Give the extent of all uninfected red blood cells.
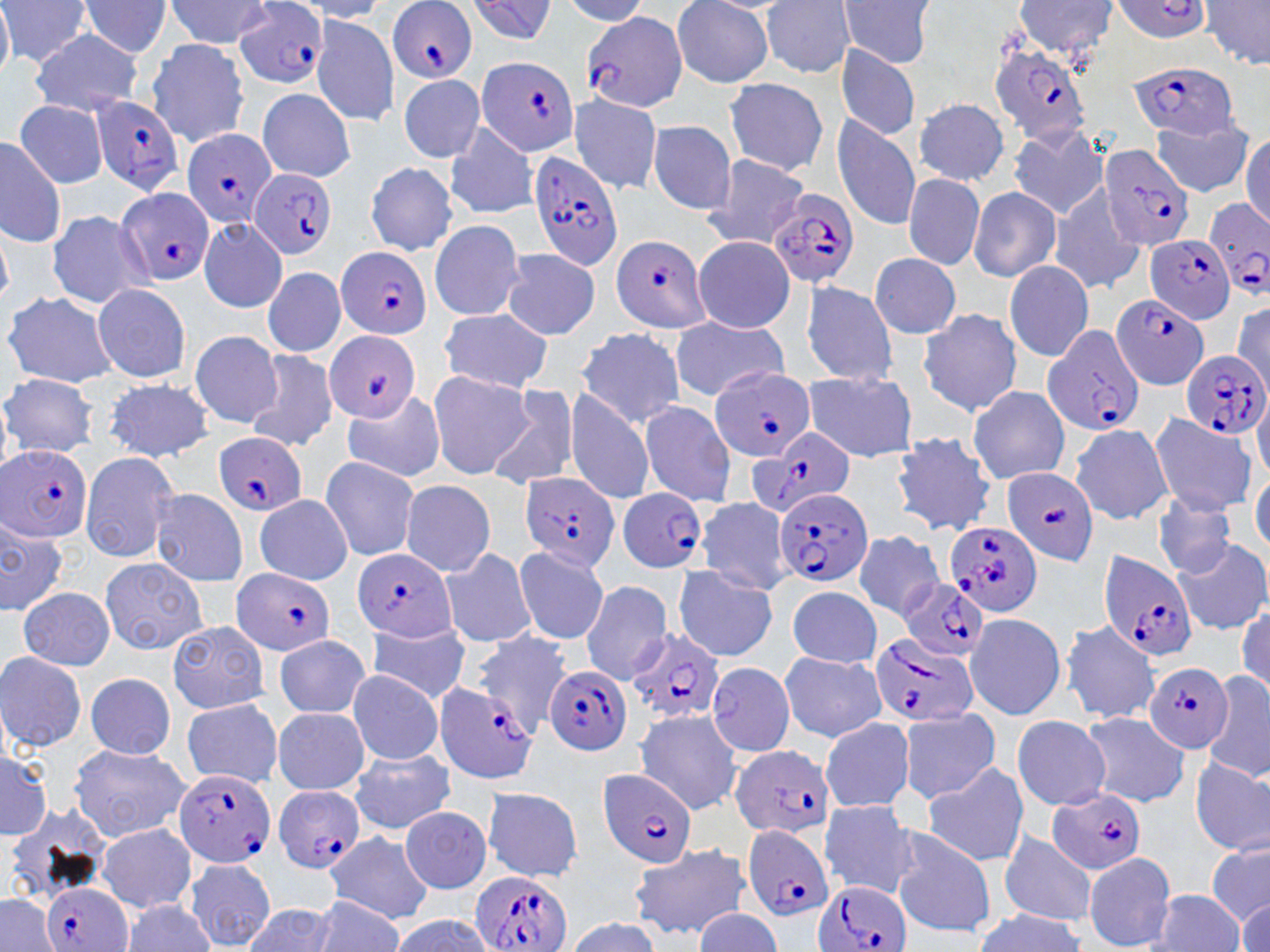

Approximate bounding boxes as named x1/y1/x2/y2 corners in pixels.
Uninfected red blood cells: (x1=80, y1=0, x2=173, y2=58), (x1=1006, y1=0, x2=1118, y2=58), (x1=2, y1=1, x2=87, y2=70), (x1=169, y1=1, x2=276, y2=46), (x1=468, y1=1, x2=562, y2=47), (x1=761, y1=1, x2=858, y2=74), (x1=1111, y1=1, x2=1214, y2=59), (x1=669, y1=2, x2=777, y2=87), (x1=834, y1=2, x2=939, y2=70), (x1=1200, y1=4, x2=1270, y2=73), (x1=314, y1=14, x2=401, y2=124), (x1=31, y1=27, x2=140, y2=118), (x1=146, y1=40, x2=251, y2=146), (x1=834, y1=43, x2=918, y2=142), (x1=393, y1=72, x2=490, y2=164), (x1=716, y1=72, x2=823, y2=172), (x1=562, y1=87, x2=662, y2=200), (x1=255, y1=91, x2=358, y2=181), (x1=912, y1=94, x2=1007, y2=185), (x1=17, y1=105, x2=113, y2=187), (x1=828, y1=109, x2=927, y2=232), (x1=434, y1=118, x2=539, y2=215), (x1=643, y1=120, x2=740, y2=220), (x1=1151, y1=124, x2=1253, y2=192), (x1=1008, y1=127, x2=1093, y2=220), (x1=1, y1=135, x2=64, y2=254), (x1=692, y1=152, x2=805, y2=253), (x1=360, y1=157, x2=454, y2=246), (x1=901, y1=175, x2=990, y2=272), (x1=1047, y1=178, x2=1145, y2=294), (x1=973, y1=183, x2=1061, y2=281), (x1=42, y1=210, x2=164, y2=299), (x1=199, y1=217, x2=288, y2=321), (x1=428, y1=221, x2=532, y2=320), (x1=688, y1=237, x2=797, y2=331), (x1=496, y1=245, x2=598, y2=337), (x1=867, y1=253, x2=965, y2=341), (x1=1006, y1=261, x2=1092, y2=361), (x1=263, y1=262, x2=343, y2=358), (x1=798, y1=274, x2=909, y2=389), (x1=90, y1=284, x2=191, y2=385), (x1=1109, y1=292, x2=1206, y2=391), (x1=7, y1=294, x2=123, y2=390), (x1=438, y1=306, x2=561, y2=393), (x1=924, y1=310, x2=1019, y2=416), (x1=671, y1=312, x2=796, y2=400), (x1=578, y1=330, x2=690, y2=423), (x1=189, y1=331, x2=286, y2=431), (x1=248, y1=349, x2=340, y2=458), (x1=429, y1=369, x2=539, y2=482), (x1=2, y1=370, x2=101, y2=460), (x1=801, y1=371, x2=921, y2=462), (x1=101, y1=375, x2=220, y2=467), (x1=490, y1=384, x2=581, y2=492), (x1=566, y1=384, x2=656, y2=505), (x1=965, y1=385, x2=1073, y2=485), (x1=335, y1=393, x2=452, y2=478), (x1=632, y1=395, x2=735, y2=508), (x1=1151, y1=410, x2=1256, y2=518), (x1=1066, y1=418, x2=1173, y2=526), (x1=894, y1=434, x2=994, y2=540), (x1=77, y1=454, x2=182, y2=565), (x1=316, y1=457, x2=423, y2=561), (x1=399, y1=481, x2=494, y2=577), (x1=147, y1=485, x2=247, y2=591), (x1=1147, y1=487, x2=1241, y2=584), (x1=696, y1=492, x2=794, y2=597), (x1=246, y1=498, x2=355, y2=589), (x1=850, y1=530, x2=945, y2=621), (x1=1164, y1=540, x2=1268, y2=638), (x1=514, y1=545, x2=615, y2=645), (x1=437, y1=547, x2=539, y2=651), (x1=97, y1=558, x2=207, y2=655), (x1=668, y1=564, x2=778, y2=661), (x1=578, y1=580, x2=670, y2=689), (x1=21, y1=583, x2=120, y2=666), (x1=784, y1=587, x2=886, y2=674), (x1=968, y1=606, x2=1071, y2=720), (x1=163, y1=620, x2=276, y2=712), (x1=1062, y1=620, x2=1138, y2=725), (x1=359, y1=621, x2=475, y2=702), (x1=478, y1=626, x2=570, y2=711), (x1=276, y1=634, x2=368, y2=715), (x1=774, y1=650, x2=891, y2=747), (x1=2, y1=652, x2=86, y2=750), (x1=707, y1=663, x2=796, y2=757), (x1=346, y1=670, x2=444, y2=764), (x1=81, y1=671, x2=173, y2=763), (x1=1204, y1=672, x2=1270, y2=778), (x1=176, y1=694, x2=284, y2=787), (x1=270, y1=705, x2=367, y2=794), (x1=899, y1=706, x2=1001, y2=804), (x1=633, y1=707, x2=750, y2=814), (x1=1086, y1=713, x2=1192, y2=807), (x1=815, y1=715, x2=919, y2=816), (x1=1008, y1=715, x2=1116, y2=812), (x1=67, y1=743, x2=189, y2=841), (x1=0, y1=751, x2=53, y2=840), (x1=348, y1=752, x2=455, y2=834), (x1=1192, y1=760, x2=1270, y2=858), (x1=919, y1=763, x2=1017, y2=862), (x1=482, y1=787, x2=577, y2=881), (x1=817, y1=801, x2=921, y2=901), (x1=398, y1=803, x2=496, y2=896), (x1=90, y1=812, x2=192, y2=911), (x1=994, y1=825, x2=1096, y2=924), (x1=894, y1=828, x2=997, y2=938), (x1=1205, y1=829, x2=1270, y2=928), (x1=342, y1=831, x2=429, y2=927), (x1=624, y1=846, x2=753, y2=934), (x1=1087, y1=852, x2=1176, y2=947), (x1=184, y1=856, x2=276, y2=945), (x1=1141, y1=889, x2=1244, y2=952), (x1=973, y1=909, x2=1087, y2=952).

Plasmodium falciparum-infected red blood cell locations: (x1=388, y1=2, x2=477, y2=80), (x1=235, y1=10, x2=330, y2=88), (x1=576, y1=14, x2=688, y2=110), (x1=472, y1=54, x2=581, y2=158), (x1=992, y1=56, x2=1090, y2=153), (x1=1124, y1=68, x2=1249, y2=137), (x1=87, y1=104, x2=184, y2=198), (x1=180, y1=130, x2=276, y2=227), (x1=1103, y1=143, x2=1197, y2=250), (x1=522, y1=149, x2=621, y2=269), (x1=250, y1=168, x2=334, y2=258), (x1=111, y1=185, x2=212, y2=287), (x1=765, y1=185, x2=856, y2=287), (x1=1201, y1=194, x2=1270, y2=299), (x1=1142, y1=233, x2=1234, y2=323), (x1=609, y1=236, x2=713, y2=333), (x1=334, y1=246, x2=432, y2=339), (x1=1039, y1=326, x2=1141, y2=431), (x1=321, y1=331, x2=425, y2=423), (x1=1179, y1=353, x2=1269, y2=439), (x1=709, y1=362, x2=822, y2=459), (x1=733, y1=430, x2=866, y2=517), (x1=210, y1=433, x2=311, y2=516), (x1=0, y1=441, x2=94, y2=550), (x1=1000, y1=466, x2=1097, y2=567), (x1=517, y1=471, x2=624, y2=576), (x1=619, y1=488, x2=704, y2=575), (x1=776, y1=488, x2=872, y2=584), (x1=947, y1=522, x2=1044, y2=618), (x1=352, y1=548, x2=460, y2=648), (x1=1096, y1=548, x2=1199, y2=657), (x1=226, y1=570, x2=344, y2=656), (x1=897, y1=577, x2=986, y2=658), (x1=621, y1=627, x2=725, y2=719), (x1=871, y1=637, x2=986, y2=724), (x1=1146, y1=658, x2=1236, y2=749), (x1=546, y1=662, x2=632, y2=757), (x1=433, y1=679, x2=531, y2=783), (x1=726, y1=744, x2=832, y2=839), (x1=171, y1=759, x2=277, y2=869), (x1=600, y1=770, x2=697, y2=872), (x1=1042, y1=783, x2=1153, y2=877), (x1=275, y1=784, x2=364, y2=872), (x1=737, y1=822, x2=835, y2=922), (x1=469, y1=864, x2=572, y2=951), (x1=40, y1=879, x2=131, y2=952), (x1=810, y1=880, x2=920, y2=952). Slide-level diagnosis: Plasmodium falciparum. 1000x magnification. One field of a larger specimen. May-Grünwald-Giemsa-stained preparation. Thin blood film. Image is 1270×952 pixels. Optical microscopy.